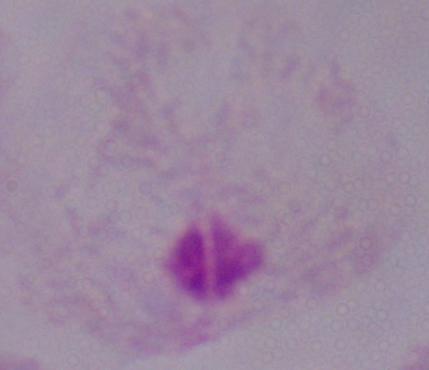 A trichomonad is seen. Photomicrograph. Captured at 1000x magnification.